Name the parasite shown.
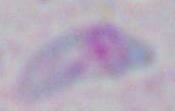

Toxoplasma gondii.

modality = micrograph
magnification = 1000x